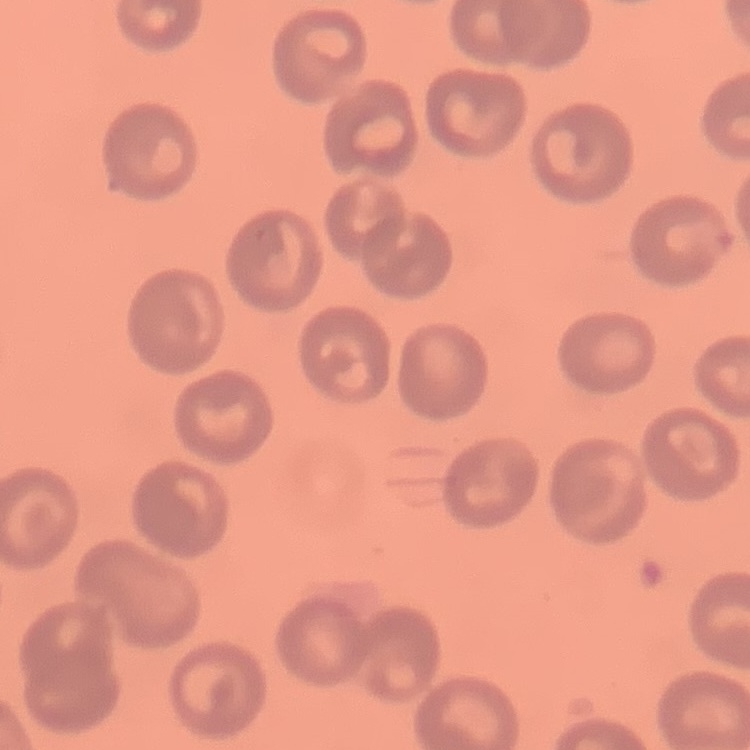
Summary:
  - Red blood cell morphology: no rouleaux formation
  - Preparation: thin blood smear
  - Image type: square crop of a larger photomicrograph
  - Stain: Field's or Giemsa